Identify the blood parasite species.
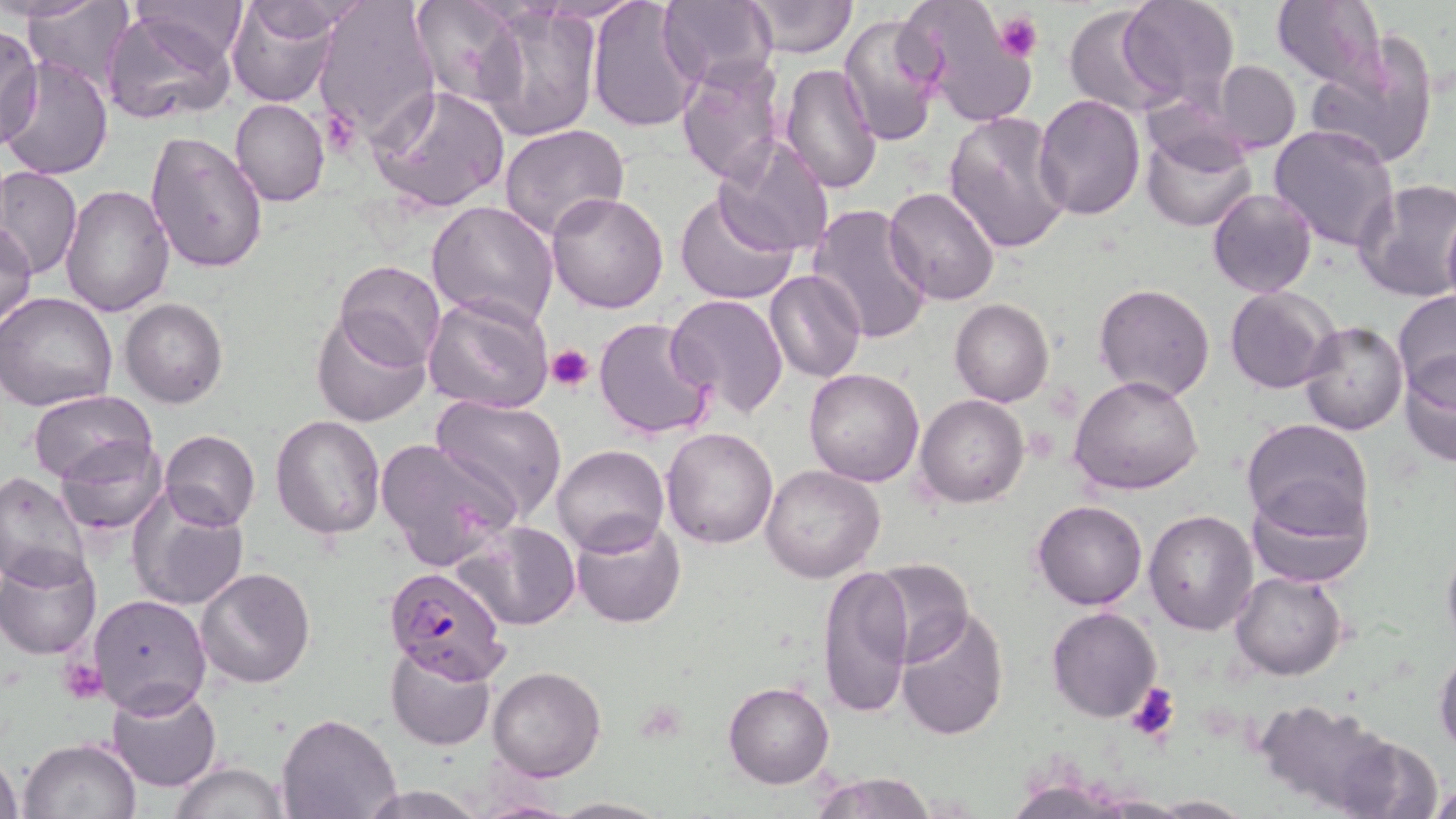
Plasmodium falciparum.

{
  "image_size": "1456×819 pixels",
  "stain": "May-Grünwald-Giemsa",
  "plasmodium_falciparum_infected_red_blood_cell_locations": "approximate bounding boxes as [x1, y1, x2, y2] in pixels: [385, 565, 509, 684]",
  "platelet_locations": "approximate bounding boxes as [x1, y1, x2, y2] in pixels: [995, 14, 1044, 63], [545, 343, 595, 392], [60, 658, 107, 705], [1125, 683, 1180, 741]",
  "preparation": "thin blood film",
  "uninfected_red_blood_cell_locations": "approximate bounding boxes as [x1, y1, x2, y2] in pixels: [3, 0, 105, 22], [128, 0, 249, 66], [226, 0, 341, 108], [312, 0, 438, 145], [405, 0, 521, 108], [898, 0, 1038, 128], [1118, 0, 1238, 108], [21, 1, 138, 91], [238, 1, 367, 44], [587, 1, 705, 132], [657, 1, 777, 89], [745, 1, 855, 57], [1270, 1, 1388, 92], [1062, 5, 1173, 115], [475, 6, 602, 141], [101, 8, 238, 125], [838, 12, 944, 147], [0, 24, 42, 147], [1305, 35, 1440, 172], [4, 55, 113, 181], [675, 55, 789, 186], [1213, 60, 1300, 154], [779, 63, 881, 194], [368, 84, 510, 213], [1033, 95, 1147, 220], [230, 97, 328, 207], [942, 111, 1072, 255], [1269, 123, 1398, 252], [499, 124, 629, 241], [1140, 129, 1255, 232], [145, 130, 270, 274], [713, 138, 835, 259], [1, 167, 81, 279], [1354, 179, 1456, 302], [60, 186, 175, 317], [882, 186, 1000, 306], [1206, 187, 1317, 298], [674, 190, 800, 308], [545, 191, 669, 312], [427, 200, 559, 329], [807, 204, 934, 345], [1441, 206, 1456, 308], [1, 221, 37, 330], [335, 260, 445, 371], [776, 262, 886, 481], [765, 269, 865, 383], [1094, 283, 1216, 402], [1225, 287, 1340, 395], [1393, 290, 1456, 398], [0, 292, 118, 413], [423, 293, 555, 414], [665, 294, 790, 419], [120, 297, 228, 409], [950, 299, 1054, 406], [312, 312, 431, 426], [593, 316, 718, 440], [1299, 322, 1408, 436], [1398, 351, 1456, 468], [804, 366, 925, 486], [1069, 375, 1204, 496], [28, 389, 157, 485], [431, 394, 567, 519], [917, 395, 1029, 508], [271, 414, 386, 539], [1241, 417, 1374, 535], [662, 427, 779, 549], [159, 429, 261, 530], [55, 436, 168, 535], [376, 439, 519, 569], [552, 444, 669, 556], [761, 465, 885, 583], [0, 472, 91, 588], [1245, 480, 1373, 589], [127, 491, 251, 611], [1032, 499, 1147, 609], [1143, 510, 1259, 634], [570, 515, 688, 626], [456, 519, 581, 631], [1440, 531, 1456, 658], [0, 548, 102, 658], [869, 559, 974, 668], [817, 564, 914, 719], [194, 568, 316, 688], [1229, 571, 1347, 679], [88, 593, 212, 717], [895, 605, 1010, 740], [1047, 607, 1160, 723], [386, 644, 497, 752], [1434, 647, 1456, 756], [488, 666, 605, 781], [106, 682, 223, 792], [723, 682, 833, 787], [1255, 700, 1409, 816], [276, 712, 401, 818], [18, 737, 143, 819], [0, 752, 22, 818], [170, 761, 291, 819], [809, 772, 939, 819], [357, 785, 492, 819], [1429, 785, 1456, 819], [1143, 795, 1252, 817], [549, 798, 669, 818]",
  "field_of_view": "one of a larger specimen",
  "magnification": "1000x",
  "modality": "optical microscopy"
}